Locate every white blood cell.
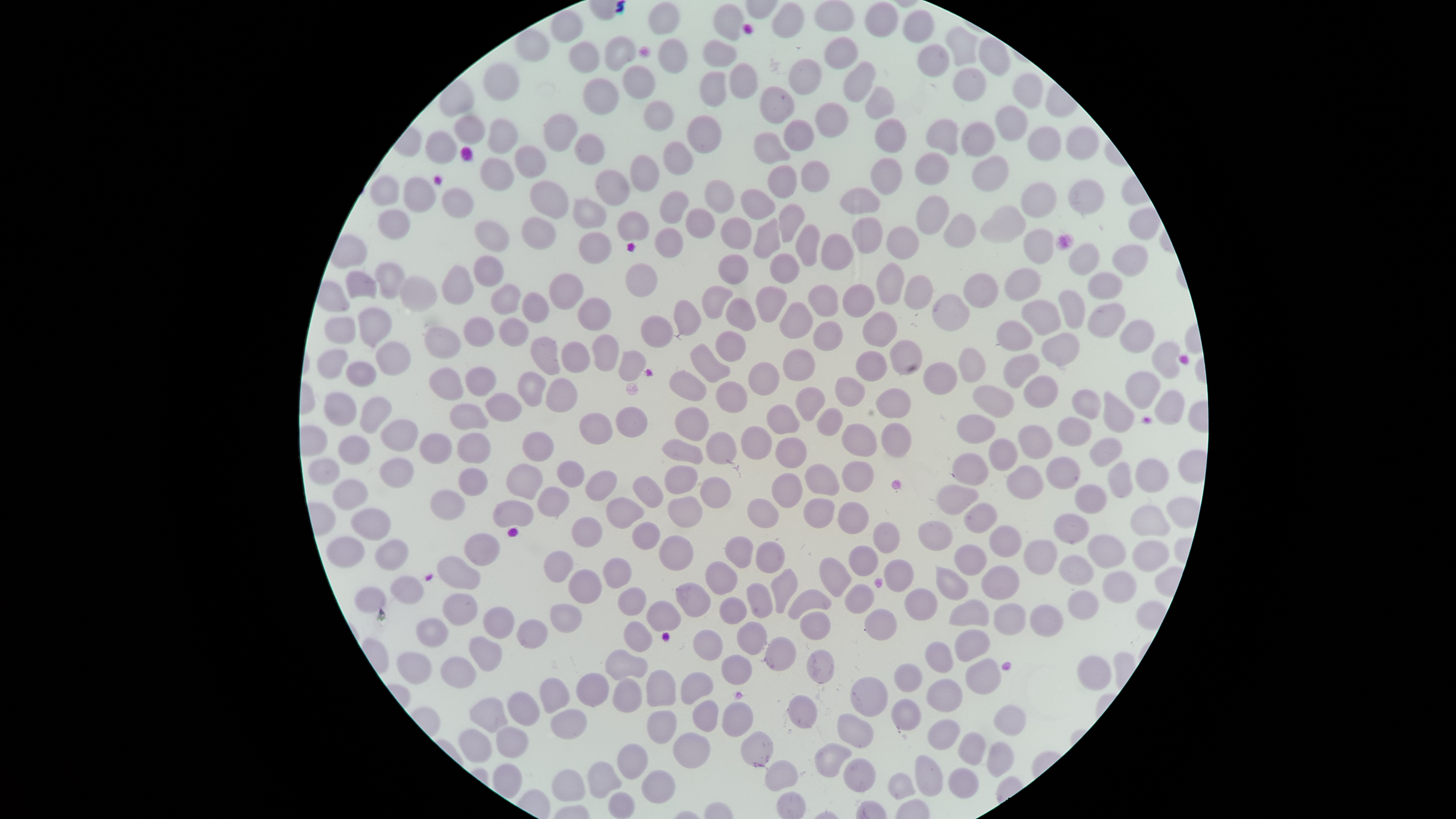
No white blood cells identified.

{
  "presence": "no malaria parasites identified",
  "uninfected_red_blood_cells": "approximate bounding boxes as (left, top, right, bottom) in pixels: (813, 0, 856, 32), (647, 1, 681, 35), (771, 1, 806, 38), (864, 1, 899, 38), (712, 3, 745, 41), (550, 8, 584, 43), (901, 9, 935, 44), (944, 24, 980, 67), (514, 27, 550, 63), (604, 35, 638, 72), (978, 35, 1011, 77), (824, 36, 858, 70), (657, 37, 688, 73), (702, 39, 738, 67), (569, 40, 600, 73), (916, 44, 950, 77), (786, 58, 822, 95), (842, 60, 876, 104), (729, 61, 759, 99), (483, 62, 520, 101), (622, 63, 657, 100), (953, 66, 986, 101), (699, 70, 727, 107), (1012, 72, 1044, 109), (582, 77, 619, 115), (759, 85, 796, 124), (864, 85, 896, 121), (643, 98, 675, 132), (814, 101, 849, 137), (993, 105, 1030, 142), (543, 113, 579, 152), (686, 114, 723, 154), (453, 115, 485, 144), (487, 117, 519, 154), (874, 118, 907, 153), (926, 118, 960, 155), (783, 119, 815, 152), (960, 121, 996, 157), (1026, 125, 1062, 161), (1065, 126, 1100, 160), (423, 130, 458, 164), (753, 131, 791, 165), (574, 133, 606, 166), (662, 139, 695, 175), (513, 144, 547, 177), (914, 151, 950, 186), (630, 153, 661, 192), (972, 154, 1010, 192), (479, 156, 515, 191), (869, 157, 903, 195), (800, 159, 830, 193), (766, 164, 798, 199), (594, 168, 631, 207), (369, 173, 400, 207), (402, 176, 436, 213), (1066, 178, 1105, 215), (704, 179, 735, 213), (529, 180, 570, 220), (1021, 181, 1058, 219), (838, 186, 881, 215), (441, 187, 475, 219), (740, 187, 776, 221), (659, 190, 690, 224), (915, 194, 950, 235), (571, 195, 607, 228), (777, 202, 806, 242), (979, 204, 1026, 244), (685, 207, 716, 238), (1128, 207, 1162, 240), (377, 208, 410, 240), (616, 210, 650, 242), (942, 213, 977, 248), (521, 215, 557, 250), (720, 215, 753, 250), (752, 216, 782, 259), (851, 216, 884, 255), (473, 220, 510, 252), (794, 223, 821, 266), (885, 225, 920, 260), (654, 227, 683, 258), (1023, 229, 1054, 265), (577, 231, 612, 264), (820, 232, 854, 271), (1067, 242, 1101, 276), (1110, 244, 1150, 277), (769, 252, 800, 284), (718, 253, 750, 285), (472, 255, 504, 287), (374, 261, 406, 299), (624, 262, 658, 297), (876, 262, 906, 306), (441, 263, 475, 305), (1004, 268, 1041, 302), (345, 270, 378, 300), (548, 272, 584, 310), (963, 272, 999, 308), (1087, 272, 1123, 299), (903, 273, 935, 311), (399, 274, 438, 312), (490, 282, 522, 314), (842, 283, 875, 317), (701, 284, 735, 320), (755, 284, 789, 323), (807, 284, 839, 318), (1057, 290, 1086, 329), (522, 291, 550, 323), (932, 292, 970, 333), (577, 297, 612, 331), (725, 297, 757, 331), (672, 298, 702, 336), (778, 300, 814, 339), (1020, 300, 1062, 336), (1087, 302, 1127, 338), (357, 306, 393, 348), (862, 310, 898, 347), (640, 314, 674, 348), (324, 316, 356, 345), (463, 316, 495, 347), (498, 317, 530, 347), (812, 319, 844, 351), (995, 319, 1033, 351), (1119, 320, 1155, 353), (424, 325, 462, 359), (714, 330, 747, 362), (1040, 332, 1080, 367), (590, 333, 620, 371), (529, 335, 561, 376), (561, 340, 590, 373), (889, 340, 923, 375), (374, 341, 411, 377), (1151, 341, 1182, 379), (690, 343, 731, 383), (958, 347, 986, 383), (316, 348, 349, 378), (782, 348, 816, 382), (618, 349, 647, 381), (856, 350, 888, 382), (1002, 353, 1041, 389), (345, 361, 377, 387), (747, 361, 781, 395), (923, 361, 957, 395), (428, 366, 464, 401), (464, 366, 497, 396), (669, 369, 707, 402), (516, 370, 547, 407), (1124, 371, 1162, 410), (1022, 374, 1059, 409), (835, 376, 866, 407), (545, 377, 578, 413), (715, 380, 748, 412), (972, 384, 1015, 419), (795, 386, 825, 421), (875, 387, 913, 419), (1071, 388, 1102, 419), (1154, 389, 1186, 425), (1102, 390, 1134, 433), (323, 391, 357, 427), (484, 392, 523, 422), (359, 396, 393, 435), (448, 402, 489, 431), (766, 403, 801, 435), (615, 406, 648, 437), (674, 406, 709, 442), (816, 406, 844, 436), (579, 412, 613, 445), (956, 414, 997, 444), (1056, 415, 1093, 447), (380, 418, 419, 452), (841, 422, 879, 457), (880, 422, 912, 458), (1017, 424, 1054, 459), (739, 425, 773, 459), (419, 431, 453, 465), (521, 431, 554, 461), (705, 431, 738, 465), (456, 432, 491, 464), (337, 435, 371, 465), (774, 436, 808, 468), (661, 437, 705, 465), (986, 437, 1018, 471), (1088, 437, 1123, 468), (951, 453, 989, 486), (1045, 456, 1080, 490), (308, 457, 342, 485), (379, 457, 415, 488), (1134, 458, 1170, 493), (556, 459, 585, 488), (841, 460, 874, 492), (1107, 461, 1133, 498), (505, 462, 544, 501), (804, 462, 841, 496), (664, 464, 698, 494), (1006, 464, 1045, 500), (458, 466, 488, 497), (584, 470, 618, 502), (770, 472, 804, 508), (631, 475, 664, 509), (699, 475, 732, 508), (332, 479, 369, 511), (935, 483, 980, 515), (1074, 484, 1107, 515), (537, 485, 571, 517), (430, 488, 466, 520), (667, 495, 704, 528), (606, 496, 645, 529), (492, 498, 535, 528), (747, 498, 779, 528), (803, 498, 835, 528), (837, 501, 870, 534), (963, 502, 998, 534), (1129, 504, 1171, 537), (351, 507, 392, 541), (1053, 513, 1090, 544), (571, 516, 603, 548), (917, 520, 954, 552), (631, 521, 661, 550), (872, 521, 900, 554), (989, 524, 1023, 558), (464, 532, 500, 566), (658, 534, 695, 570), (724, 534, 754, 569), (1087, 534, 1127, 568), (325, 536, 366, 568), (375, 539, 410, 571), (1022, 539, 1058, 576), (755, 540, 787, 573), (1131, 540, 1170, 572), (954, 543, 987, 575), (848, 545, 879, 577), (542, 550, 574, 583), (1059, 555, 1096, 587), (436, 556, 481, 589), (819, 556, 852, 598), (601, 557, 633, 588), (883, 559, 915, 593), (704, 561, 739, 596), (936, 565, 969, 601), (981, 565, 1020, 600), (770, 567, 798, 614), (568, 568, 603, 605), (1102, 571, 1137, 605), (389, 575, 424, 605), (674, 581, 712, 618), (746, 582, 774, 618), (844, 583, 875, 614), (354, 586, 388, 613), (617, 586, 647, 616), (904, 587, 938, 621), (787, 588, 832, 620), (1066, 590, 1099, 621), (442, 592, 478, 626), (719, 596, 748, 625), (948, 598, 989, 627), (645, 600, 682, 632), (549, 602, 583, 633), (992, 603, 1027, 636), (1029, 604, 1064, 637), (483, 605, 516, 639), (863, 608, 897, 640), (799, 611, 831, 641), (416, 617, 449, 647), (516, 618, 549, 649), (623, 620, 654, 652), (736, 621, 768, 655), (693, 628, 724, 661), (953, 629, 991, 662), (468, 635, 503, 672), (764, 636, 797, 671), (924, 640, 954, 673), (605, 648, 648, 680), (807, 649, 835, 684), (396, 651, 433, 685), (720, 654, 753, 685), (1076, 655, 1112, 691), (440, 656, 477, 688), (964, 658, 1002, 694), (893, 663, 923, 692), (645, 669, 677, 707), (680, 671, 714, 705), (575, 673, 609, 706), (850, 675, 889, 717), (538, 676, 571, 714), (611, 678, 642, 713), (925, 678, 963, 713), (506, 691, 541, 727), (786, 694, 818, 728), (469, 697, 510, 733), (691, 698, 719, 732), (890, 698, 922, 731), (721, 701, 754, 737), (993, 704, 1027, 735), (550, 708, 588, 739), (646, 710, 677, 744), (836, 712, 874, 749), (927, 718, 960, 750), (495, 725, 529, 758), (457, 728, 493, 763), (739, 730, 773, 768), (672, 731, 711, 769), (957, 731, 987, 765), (986, 740, 1015, 778), (617, 742, 648, 780), (814, 742, 853, 777), (914, 754, 944, 797), (843, 757, 876, 792), (764, 759, 799, 791), (587, 760, 623, 799), (493, 762, 523, 799), (947, 767, 980, 798), (551, 769, 585, 801), (641, 770, 676, 804), (887, 772, 916, 799), (608, 790, 635, 819)",
  "preparation": "thin blood film",
  "stain": "Giemsa",
  "visible_region": "circular",
  "image_size": "1456×819 pixels",
  "capture": "smartphone photograph through the microscope eyepiece",
  "field_of_view": "single"
}